Give the position of every Plasmodium parasite.
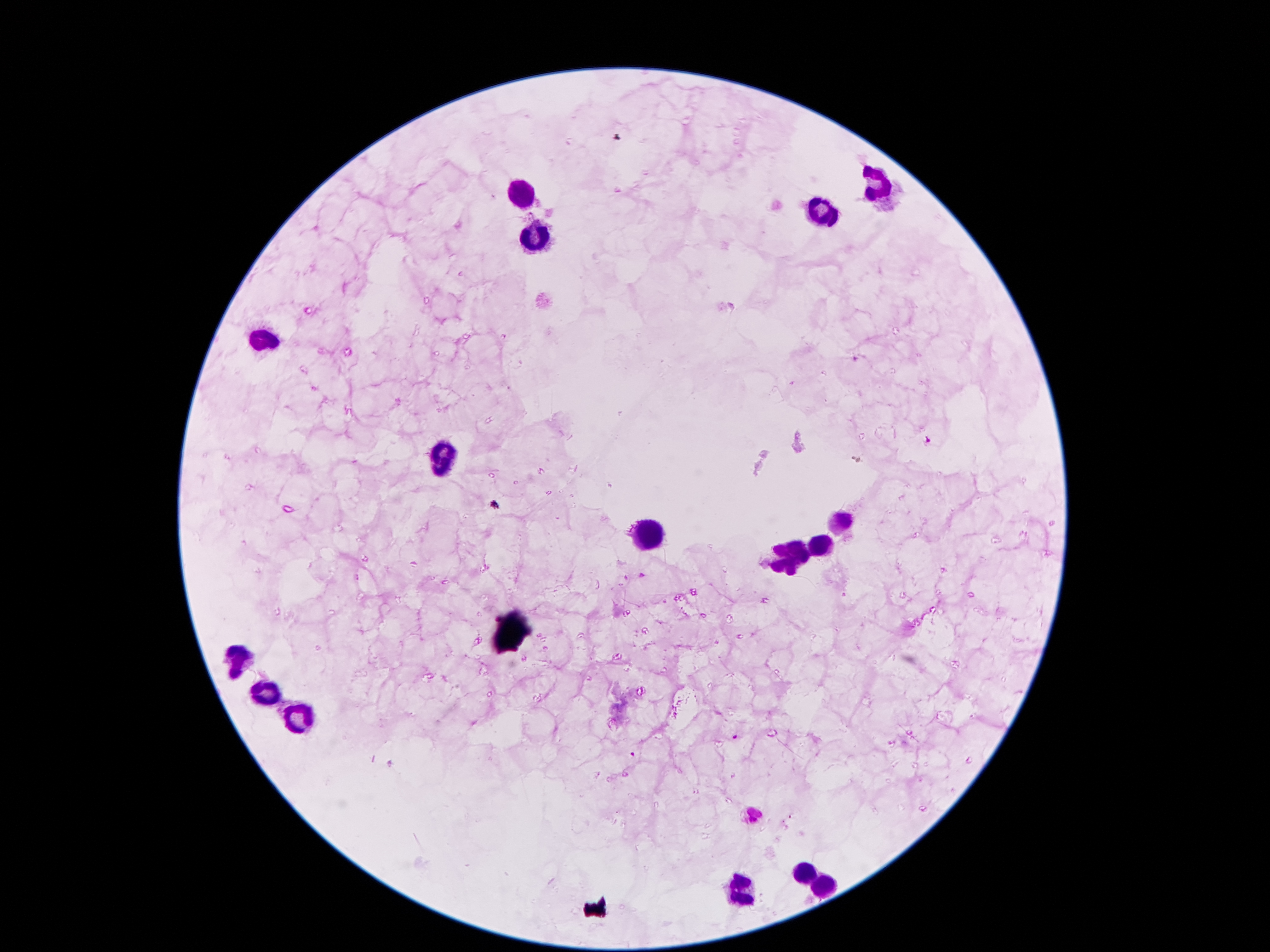
Approximate object centers, in pixels from the top-left corner.
Plasmodium parasites: (x=856, y=359), (x=928, y=438), (x=734, y=736), (x=634, y=755).

Summary:
  - Leukocyte locations: (x=877, y=183), (x=523, y=200), (x=826, y=211), (x=539, y=239), (x=444, y=458), (x=837, y=519), (x=645, y=532), (x=822, y=547), (x=790, y=555), (x=241, y=657), (x=262, y=692), (x=299, y=717), (x=804, y=873), (x=819, y=885), (x=738, y=891)
  - Preparation: thick peripheral-blood smear
  - Capture: smartphone through the microscope eyepiece
  - Patient malaria status: positive for Plasmodium falciparum
  - Stain: Giemsa
  - Field of view: single
  - Magnification: 100x
  - Image size: 1270×952 pixels